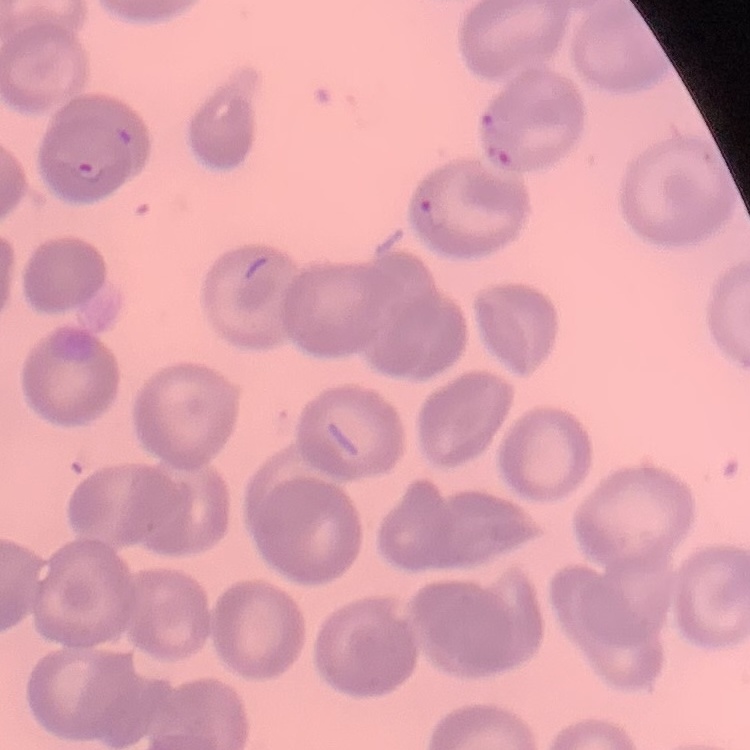 The red blood cells show no rouleaux formation. Thin peripheral smear. One tile cut from a larger photomicrograph. Field's or Giemsa stain.